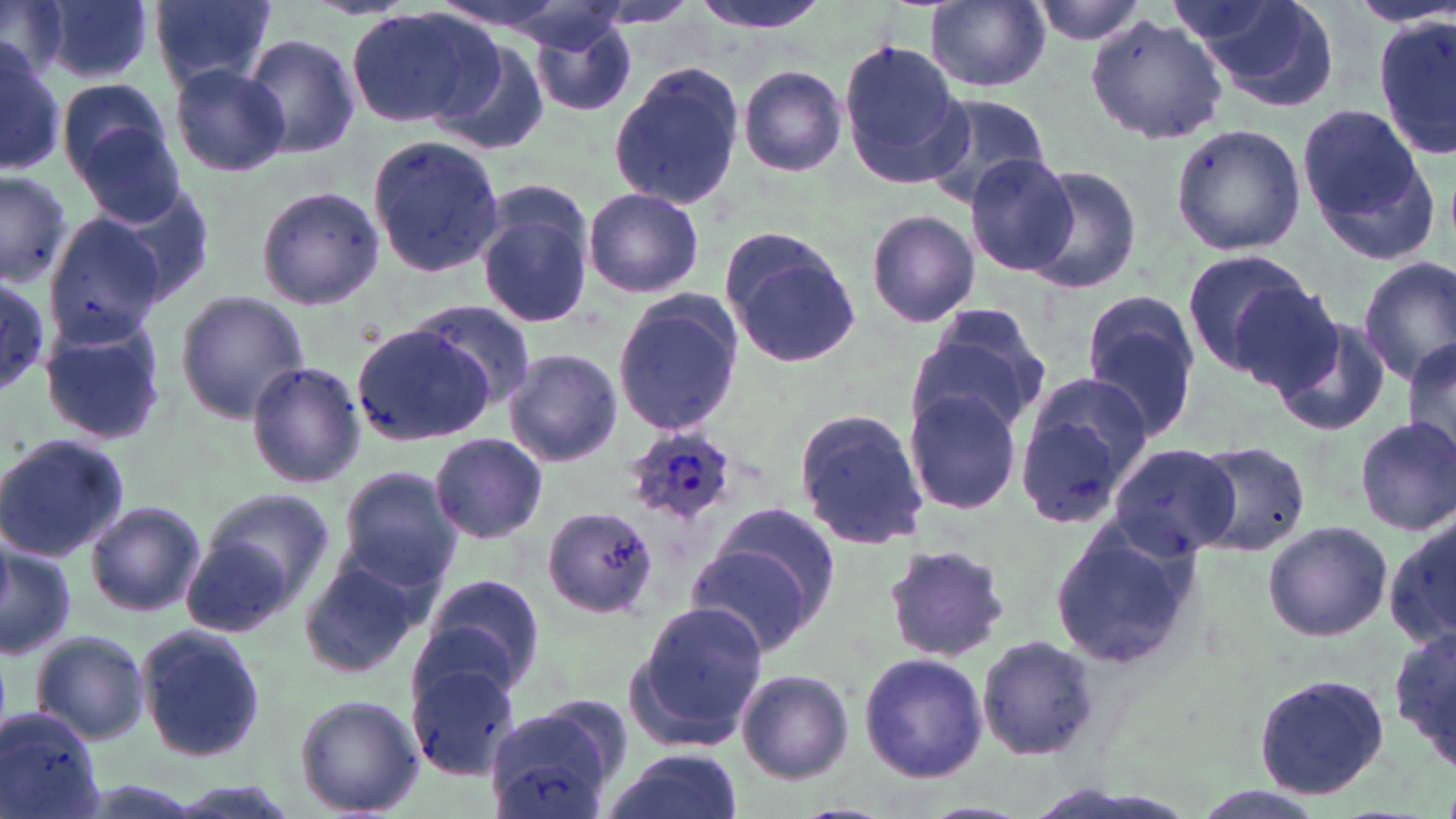

slide-level diagnosis = Plasmodium ovale
preparation = thin blood film
modality = light microscopy
uninfected red blood cell locations = approximate bounding boxes as (x1, y1, x2, y2) in pixels: (2, 0, 66, 74), (149, 0, 279, 91), (687, 0, 831, 36), (926, 0, 1050, 91), (1030, 0, 1149, 45), (1183, 0, 1342, 107), (41, 1, 156, 86), (347, 8, 500, 130), (530, 14, 639, 119), (1086, 14, 1228, 143), (1375, 15, 1454, 164), (242, 34, 361, 160), (431, 38, 550, 155), (0, 40, 64, 177), (837, 41, 966, 184), (610, 60, 746, 209), (168, 63, 290, 177), (738, 65, 847, 176), (58, 77, 177, 188), (912, 92, 1053, 209), (1296, 103, 1433, 254), (78, 124, 190, 228), (1170, 125, 1306, 257), (367, 132, 503, 279), (963, 156, 1079, 278), (1021, 164, 1143, 295), (0, 168, 73, 292), (98, 181, 212, 307), (254, 184, 384, 313), (583, 188, 704, 299), (477, 197, 595, 330), (864, 208, 981, 327), (43, 211, 167, 342), (720, 230, 861, 367), (1180, 251, 1321, 380), (1357, 257, 1456, 388), (0, 274, 52, 389), (1227, 280, 1354, 402), (174, 289, 309, 425), (611, 289, 744, 441), (404, 299, 540, 415), (1080, 301, 1202, 441), (908, 306, 1051, 440), (1271, 316, 1391, 438), (37, 318, 167, 448), (351, 322, 495, 448), (1401, 338, 1456, 465), (503, 349, 624, 467), (245, 360, 365, 491), (1015, 372, 1157, 520), (908, 388, 1026, 514), (794, 410, 928, 551), (1353, 416, 1456, 536), (429, 433, 549, 544), (0, 434, 128, 561), (1194, 441, 1310, 556), (1107, 442, 1241, 558), (337, 468, 465, 590), (202, 486, 335, 604), (84, 500, 206, 618), (545, 505, 658, 616), (689, 514, 836, 654), (1385, 516, 1456, 650), (1047, 518, 1203, 671), (1262, 520, 1392, 643), (181, 528, 310, 639), (0, 540, 77, 663), (884, 543, 1012, 664), (295, 558, 427, 680), (417, 574, 546, 700), (626, 601, 767, 750), (1390, 623, 1456, 769), (137, 624, 267, 763), (28, 629, 151, 747), (977, 634, 1100, 759), (856, 651, 990, 782), (404, 661, 520, 780), (735, 668, 854, 785), (1250, 673, 1390, 800), (294, 693, 425, 816), (487, 695, 633, 819), (0, 703, 108, 819), (600, 751, 745, 819), (155, 781, 304, 819)
magnification = 1000x
field of view = one of a larger specimen
stain = May-Grünwald-Giemsa
Plasmodium ovale-infected red blood cell locations = approximate bounding boxes as (x1, y1, x2, y2) in pixels: (624, 427, 735, 526)
image size = 1456×819 pixels